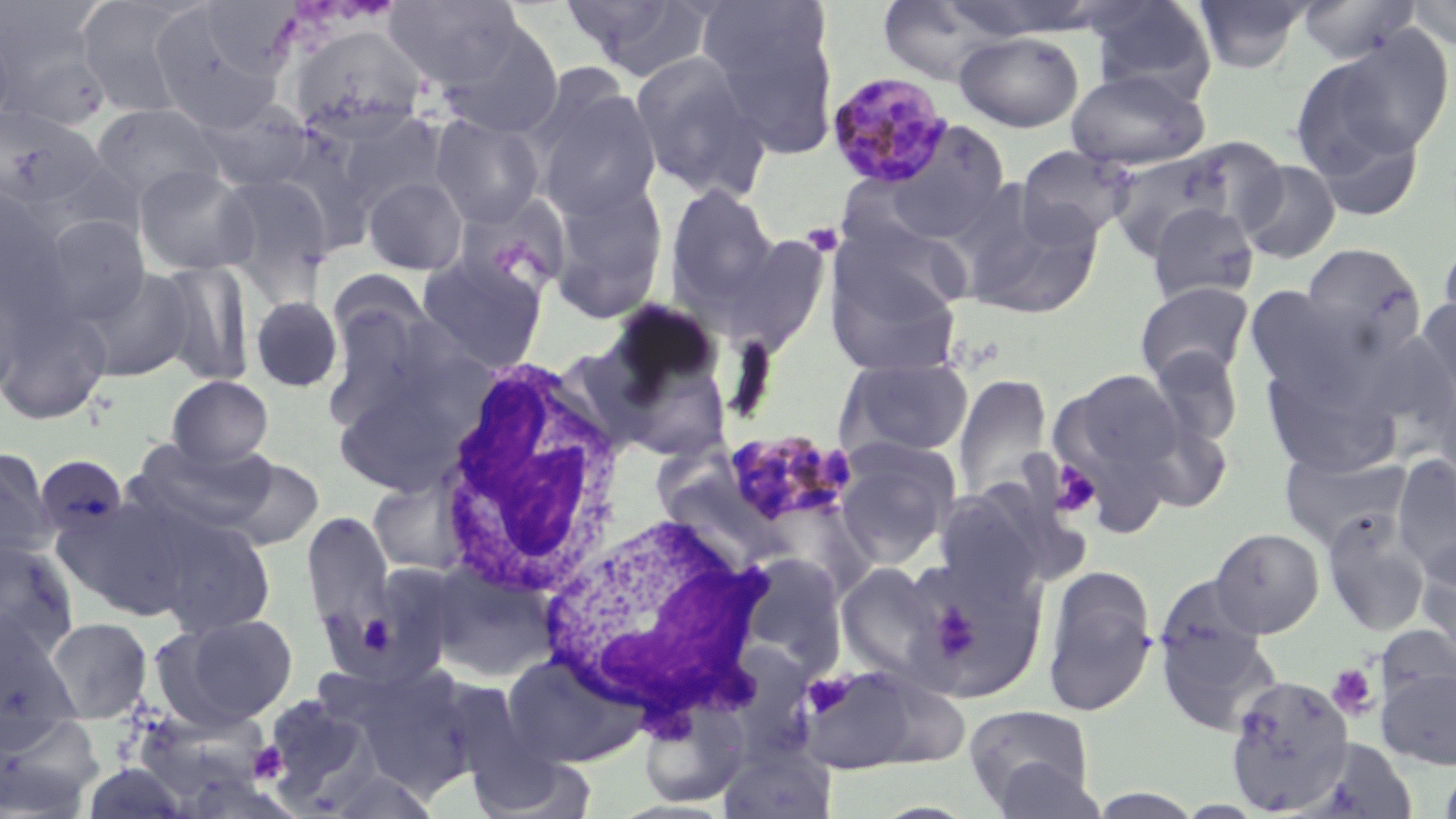
Summary:
  - Coordinate format: approximate bounding boxes as (x1, y1, x2, y2) in pixels
  - Plasmodium malariae-infected red blood cell locations: (826, 70, 954, 191), (720, 429, 858, 531)
  - Platelet locations (subset): (803, 225, 847, 257), (1050, 461, 1101, 517), (1327, 664, 1378, 718), (806, 673, 853, 717), (249, 742, 288, 784)
  - Uninfected red blood cell locations (subset): (76, 0, 202, 117), (384, 0, 526, 90), (560, 0, 716, 81), (875, 0, 1013, 85), (1083, 0, 1217, 100), (1192, 0, 1313, 74), (1296, 0, 1421, 64), (1403, 0, 1456, 49), (148, 4, 288, 132), (702, 4, 839, 159), (0, 5, 114, 132), (0, 18, 16, 136), (435, 19, 565, 140), (286, 24, 431, 142), (953, 31, 1084, 132), (1304, 31, 1455, 166), (629, 51, 772, 202), (1067, 68, 1209, 171), (532, 83, 663, 222), (191, 98, 318, 194), (90, 102, 225, 208), (0, 105, 103, 213), (331, 110, 444, 215), (430, 113, 546, 228), (1307, 118, 1427, 224), (876, 119, 1011, 243), (1177, 137, 1289, 239), (1015, 144, 1138, 246), (1106, 147, 1241, 259), (1238, 160, 1341, 264), (133, 164, 259, 276), (213, 172, 335, 297), (363, 175, 469, 275), (547, 181, 669, 322), (663, 183, 781, 314), (0, 187, 68, 317), (956, 188, 1102, 318), (1146, 203, 1259, 304), (39, 213, 151, 327), (829, 217, 972, 328), (715, 233, 831, 357), (1437, 235, 1456, 339), (1301, 243, 1426, 359), (416, 254, 549, 373), (823, 255, 964, 378), (153, 259, 255, 386), (79, 266, 195, 382), (325, 268, 434, 365), (0, 281, 23, 403), (1135, 282, 1255, 385), (1244, 285, 1367, 397), (322, 293, 447, 432), (249, 295, 344, 393), (1415, 296, 1456, 401), (0, 302, 113, 425), (591, 307, 735, 463), (1145, 345, 1245, 451), (836, 356, 975, 461), (1262, 363, 1400, 478), (1052, 367, 1187, 498), (331, 370, 475, 498), (952, 374, 1054, 505), (166, 375, 274, 468), (1432, 379, 1456, 487), (1128, 411, 1234, 515), (128, 438, 276, 538), (832, 440, 959, 566), (0, 447, 56, 565), (1281, 449, 1409, 549), (1391, 454, 1456, 581), (33, 455, 130, 544), (221, 455, 324, 552), (367, 477, 473, 578), (933, 484, 1053, 603), (56, 495, 200, 622), (147, 510, 278, 639), (1321, 511, 1431, 636), (302, 512, 395, 635), (1210, 527, 1324, 637), (0, 538, 80, 659), (903, 554, 1049, 703), (1417, 555, 1456, 671), (427, 560, 560, 683), (323, 562, 464, 687), (836, 562, 949, 682), (1042, 564, 1158, 717), (1154, 611, 1282, 736), (158, 612, 300, 728), (0, 614, 80, 731), (43, 616, 154, 723), (1375, 624, 1456, 709), (503, 651, 644, 767), (802, 664, 926, 774), (1376, 668, 1456, 770), (1224, 674, 1355, 813), (262, 695, 381, 809), (639, 699, 750, 808), (963, 704, 1096, 814), (127, 711, 272, 810), (0, 715, 104, 817), (717, 742, 837, 818), (464, 745, 598, 818), (987, 758, 1109, 818), (1437, 762, 1456, 818), (327, 768, 440, 818)
  - White blood cell locations: (431, 354, 629, 602), (544, 513, 766, 723)
  - Slide-level diagnosis: Plasmodium malariae
  - Magnification: 1000x
  - Image size: 1456×819 pixels
  - Stain: May-Grünwald-Giemsa
  - Modality: light microscopy
  - Preparation: thin blood smear
  - Field of view: single